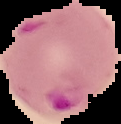
Image is 121×124 pixels. The area outside the segmented cell region is set to black. From a thin blood film. Result: malaria parasites detected.